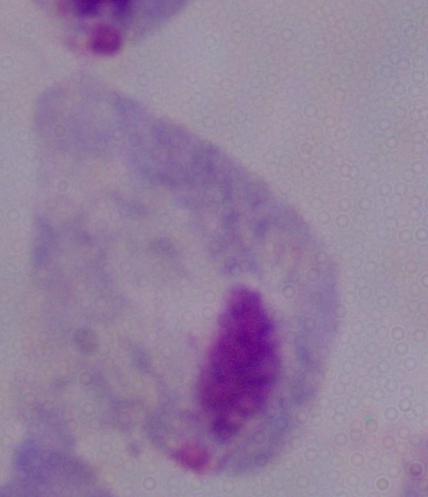

Summary:
  - Identification: trichomonad
  - Modality: micrograph
  - Magnification: 1000x